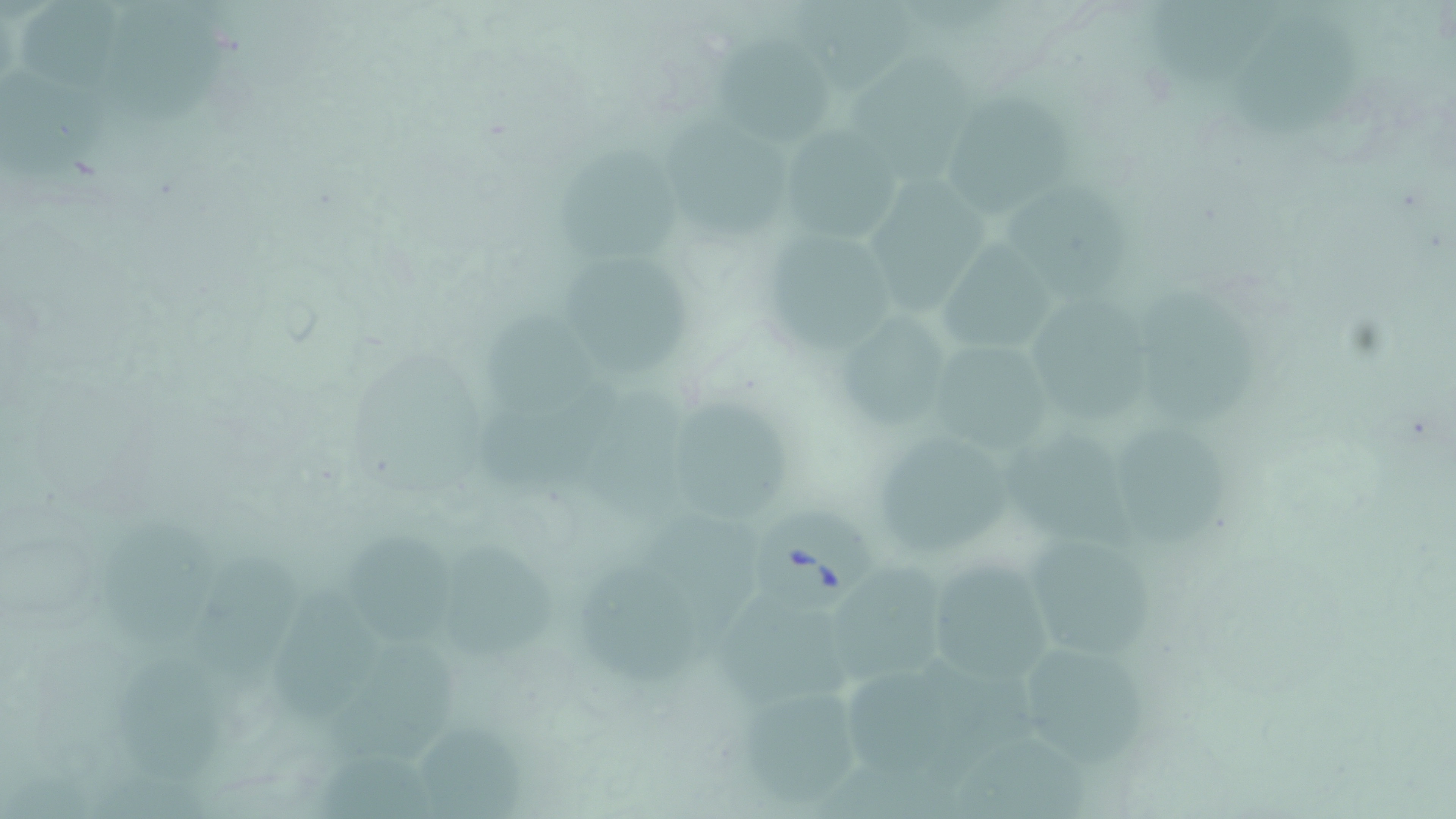
Summary:
  - Coordinate format: approximate bounding boxes as (x1,y1)-(x2,y2) corner pairs in pixels
  - Babesia divergens-infected red blood cell locations: (757,508)-(874,612)
  - Uninfected red blood cell locations: (19,0)-(119,92), (787,0)-(923,94), (1145,0)-(1291,85), (1226,15)-(1364,140), (714,32)-(831,149), (849,52)-(978,183), (951,90)-(1074,217), (669,116)-(791,241), (786,124)-(903,244), (559,145)-(683,261), (866,171)-(987,315), (1007,183)-(1132,312), (755,230)-(899,358), (933,233)-(1062,349), (565,261)-(692,379), (1136,285)-(1259,425), (1033,295)-(1150,424), (483,310)-(596,424), (837,314)-(945,424), (923,337)-(1059,458), (584,384)-(692,536), (674,403)-(792,519), (1116,422)-(1236,548), (1004,425)-(1131,548), (883,439)-(1029,556), (105,514)-(220,643), (344,529)-(455,648), (1013,531)-(1162,662), (441,540)-(556,659), (204,551)-(300,699), (923,555)-(1060,685), (581,557)-(714,688), (829,567)-(949,686), (272,577)-(375,726), (719,591)-(854,696), (326,637)-(461,766), (1024,643)-(1153,770), (113,655)-(223,783), (727,682)-(865,808), (414,712)-(523,819), (951,726)-(1090,816)
  - Slide-level diagnosis: Babesia divergens
  - Magnification: 1000x
  - Modality: optical microscopy
  - Stain: May-Grünwald-Giemsa
  - Field of view: single
  - Image size: 1456×819 pixels
  - Preparation: thin blood film